Assess this cell for malaria.
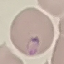

It is parasitized.

{
  "capture": "smartphone camera at the microscope eyepiece",
  "stain": "Giemsa",
  "preparation": "thin blood smear",
  "image_type": "cell patch, automatically extracted from a larger field of view and resized to 64 × 64 pixels"
}